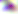

modality = micrograph
magnification = 400x
identification = Toxoplasma gondii